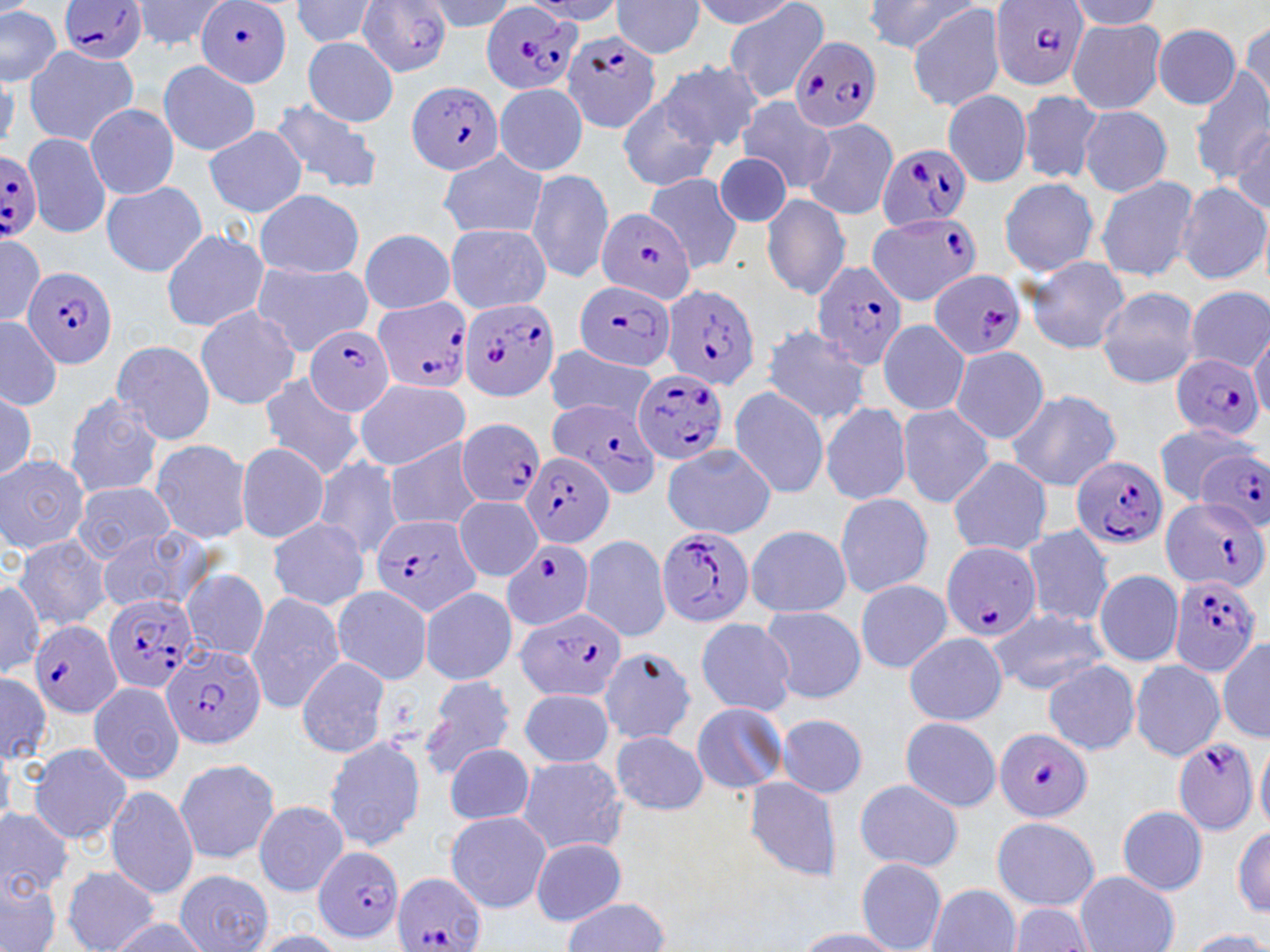

slide-level diagnosis = Plasmodium falciparum
field of view = single
image size = 1270×952 pixels
preparation = thin blood smear
uninfected red blood cell locations = approximate bounding boxes as named x1/y1/x2/y2 corners in pixels: (x1=129, y1=0, x2=230, y2=53), (x1=288, y1=0, x2=385, y2=48), (x1=420, y1=0, x2=516, y2=32), (x1=689, y1=0, x2=798, y2=33), (x1=723, y1=0, x2=830, y2=104), (x1=867, y1=0, x2=975, y2=54), (x1=610, y1=1, x2=705, y2=59), (x1=1064, y1=2, x2=1167, y2=31), (x1=906, y1=3, x2=1008, y2=112), (x1=0, y1=6, x2=62, y2=86), (x1=1067, y1=17, x2=1168, y2=115), (x1=1238, y1=19, x2=1269, y2=111), (x1=1152, y1=25, x2=1242, y2=109), (x1=303, y1=37, x2=399, y2=127), (x1=25, y1=46, x2=138, y2=145), (x1=158, y1=59, x2=261, y2=156), (x1=657, y1=59, x2=765, y2=154), (x1=1187, y1=70, x2=1269, y2=180), (x1=494, y1=81, x2=589, y2=177), (x1=942, y1=88, x2=1033, y2=188), (x1=1017, y1=89, x2=1104, y2=185), (x1=736, y1=95, x2=831, y2=191), (x1=617, y1=96, x2=719, y2=192), (x1=268, y1=97, x2=383, y2=196), (x1=84, y1=102, x2=179, y2=200), (x1=1078, y1=106, x2=1172, y2=196), (x1=800, y1=115, x2=898, y2=220), (x1=204, y1=125, x2=308, y2=218), (x1=1229, y1=128, x2=1269, y2=209), (x1=22, y1=131, x2=111, y2=239), (x1=437, y1=150, x2=547, y2=239), (x1=711, y1=153, x2=793, y2=229), (x1=525, y1=168, x2=614, y2=282), (x1=644, y1=172, x2=742, y2=271), (x1=1093, y1=174, x2=1200, y2=283), (x1=998, y1=176, x2=1101, y2=276), (x1=101, y1=181, x2=208, y2=279), (x1=1176, y1=181, x2=1269, y2=286), (x1=255, y1=189, x2=364, y2=279), (x1=762, y1=194, x2=851, y2=299), (x1=444, y1=223, x2=551, y2=315), (x1=160, y1=227, x2=268, y2=333), (x1=359, y1=228, x2=456, y2=314), (x1=0, y1=234, x2=44, y2=328), (x1=1027, y1=256, x2=1131, y2=354), (x1=250, y1=261, x2=373, y2=356), (x1=221, y1=274, x2=335, y2=382), (x1=1096, y1=286, x2=1201, y2=390), (x1=1185, y1=287, x2=1270, y2=373), (x1=194, y1=304, x2=301, y2=410), (x1=0, y1=316, x2=63, y2=409), (x1=878, y1=319, x2=969, y2=418), (x1=760, y1=323, x2=873, y2=426), (x1=1249, y1=326, x2=1269, y2=421), (x1=109, y1=339, x2=218, y2=445), (x1=949, y1=345, x2=1050, y2=445), (x1=545, y1=346, x2=660, y2=424), (x1=258, y1=373, x2=363, y2=479), (x1=353, y1=378, x2=471, y2=470), (x1=1, y1=387, x2=37, y2=482), (x1=729, y1=387, x2=831, y2=499), (x1=1004, y1=388, x2=1122, y2=492), (x1=64, y1=393, x2=164, y2=497), (x1=818, y1=401, x2=914, y2=507), (x1=896, y1=404, x2=993, y2=508), (x1=1151, y1=423, x2=1258, y2=503), (x1=146, y1=438, x2=254, y2=544), (x1=384, y1=438, x2=484, y2=533), (x1=234, y1=442, x2=329, y2=543), (x1=662, y1=444, x2=775, y2=539), (x1=1, y1=452, x2=90, y2=553), (x1=313, y1=454, x2=405, y2=563), (x1=947, y1=458, x2=1052, y2=556), (x1=71, y1=482, x2=176, y2=563), (x1=833, y1=492, x2=934, y2=598), (x1=453, y1=496, x2=543, y2=581), (x1=268, y1=516, x2=368, y2=611), (x1=93, y1=525, x2=211, y2=615), (x1=1021, y1=525, x2=1114, y2=627), (x1=744, y1=526, x2=854, y2=616), (x1=13, y1=534, x2=112, y2=630), (x1=578, y1=534, x2=672, y2=643), (x1=179, y1=569, x2=271, y2=662), (x1=1093, y1=569, x2=1183, y2=667), (x1=0, y1=575, x2=49, y2=681), (x1=855, y1=579, x2=951, y2=673), (x1=329, y1=586, x2=435, y2=685), (x1=419, y1=586, x2=517, y2=685), (x1=245, y1=591, x2=347, y2=715), (x1=760, y1=605, x2=865, y2=705), (x1=988, y1=607, x2=1108, y2=694), (x1=694, y1=617, x2=797, y2=714), (x1=903, y1=631, x2=1007, y2=726), (x1=1217, y1=637, x2=1270, y2=742), (x1=598, y1=647, x2=698, y2=743), (x1=296, y1=655, x2=390, y2=759), (x1=1129, y1=658, x2=1226, y2=761), (x1=1042, y1=660, x2=1140, y2=755), (x1=0, y1=670, x2=52, y2=768), (x1=420, y1=674, x2=515, y2=778), (x1=87, y1=679, x2=186, y2=785), (x1=511, y1=687, x2=618, y2=771), (x1=690, y1=702, x2=787, y2=794), (x1=775, y1=713, x2=867, y2=798), (x1=899, y1=718, x2=1002, y2=812), (x1=611, y1=730, x2=709, y2=814), (x1=1255, y1=735, x2=1270, y2=832), (x1=322, y1=737, x2=428, y2=851), (x1=28, y1=742, x2=132, y2=846), (x1=443, y1=742, x2=534, y2=826), (x1=515, y1=755, x2=629, y2=856), (x1=173, y1=757, x2=282, y2=866), (x1=742, y1=777, x2=844, y2=883), (x1=854, y1=779, x2=963, y2=872), (x1=104, y1=783, x2=199, y2=900), (x1=253, y1=800, x2=349, y2=895), (x1=1116, y1=805, x2=1208, y2=895), (x1=0, y1=809, x2=73, y2=902), (x1=445, y1=811, x2=551, y2=912), (x1=991, y1=817, x2=1100, y2=911), (x1=1231, y1=821, x2=1270, y2=919), (x1=530, y1=836, x2=628, y2=925), (x1=855, y1=859, x2=948, y2=952), (x1=61, y1=866, x2=160, y2=952), (x1=174, y1=869, x2=272, y2=952), (x1=1, y1=871, x2=63, y2=952), (x1=1075, y1=872, x2=1180, y2=951), (x1=929, y1=885, x2=1021, y2=952), (x1=558, y1=899, x2=673, y2=950), (x1=1008, y1=902, x2=1093, y2=951), (x1=108, y1=915, x2=209, y2=952), (x1=791, y1=928, x2=911, y2=952), (x1=1184, y1=929, x2=1270, y2=952), (x1=245, y1=930, x2=349, y2=951)
modality = light microscopy
magnification = 1000x
Plasmodium falciparum-infected red blood cell locations = approximate bounding boxes as named x1/y1/x2/y2 corners in pixels: (x1=195, y1=0, x2=293, y2=88), (x1=359, y1=0, x2=453, y2=78), (x1=59, y1=1, x2=148, y2=64), (x1=991, y1=1, x2=1090, y2=89), (x1=478, y1=6, x2=581, y2=99), (x1=563, y1=29, x2=663, y2=133), (x1=791, y1=35, x2=881, y2=134), (x1=407, y1=82, x2=505, y2=177), (x1=878, y1=142, x2=972, y2=231), (x1=0, y1=151, x2=43, y2=239), (x1=596, y1=207, x2=694, y2=305), (x1=868, y1=212, x2=983, y2=305), (x1=810, y1=258, x2=909, y2=371), (x1=23, y1=267, x2=118, y2=370), (x1=927, y1=268, x2=1028, y2=361), (x1=572, y1=280, x2=678, y2=373), (x1=660, y1=284, x2=760, y2=392), (x1=373, y1=296, x2=473, y2=396), (x1=457, y1=299, x2=563, y2=401), (x1=307, y1=323, x2=398, y2=417), (x1=1171, y1=353, x2=1262, y2=441), (x1=632, y1=367, x2=731, y2=464), (x1=553, y1=399, x2=663, y2=502), (x1=457, y1=419, x2=544, y2=508), (x1=1196, y1=449, x2=1270, y2=529), (x1=523, y1=450, x2=614, y2=550), (x1=1073, y1=456, x2=1167, y2=551), (x1=1160, y1=497, x2=1268, y2=594), (x1=371, y1=513, x2=486, y2=616), (x1=659, y1=527, x2=755, y2=628), (x1=502, y1=539, x2=593, y2=630), (x1=940, y1=541, x2=1041, y2=645), (x1=1169, y1=573, x2=1260, y2=679), (x1=102, y1=591, x2=200, y2=695), (x1=515, y1=607, x2=626, y2=704), (x1=30, y1=620, x2=122, y2=718), (x1=161, y1=644, x2=267, y2=750), (x1=994, y1=727, x2=1093, y2=823), (x1=1172, y1=739, x2=1259, y2=835), (x1=314, y1=844, x2=405, y2=944), (x1=393, y1=872, x2=488, y2=952)
stain = May-Grünwald-Giemsa